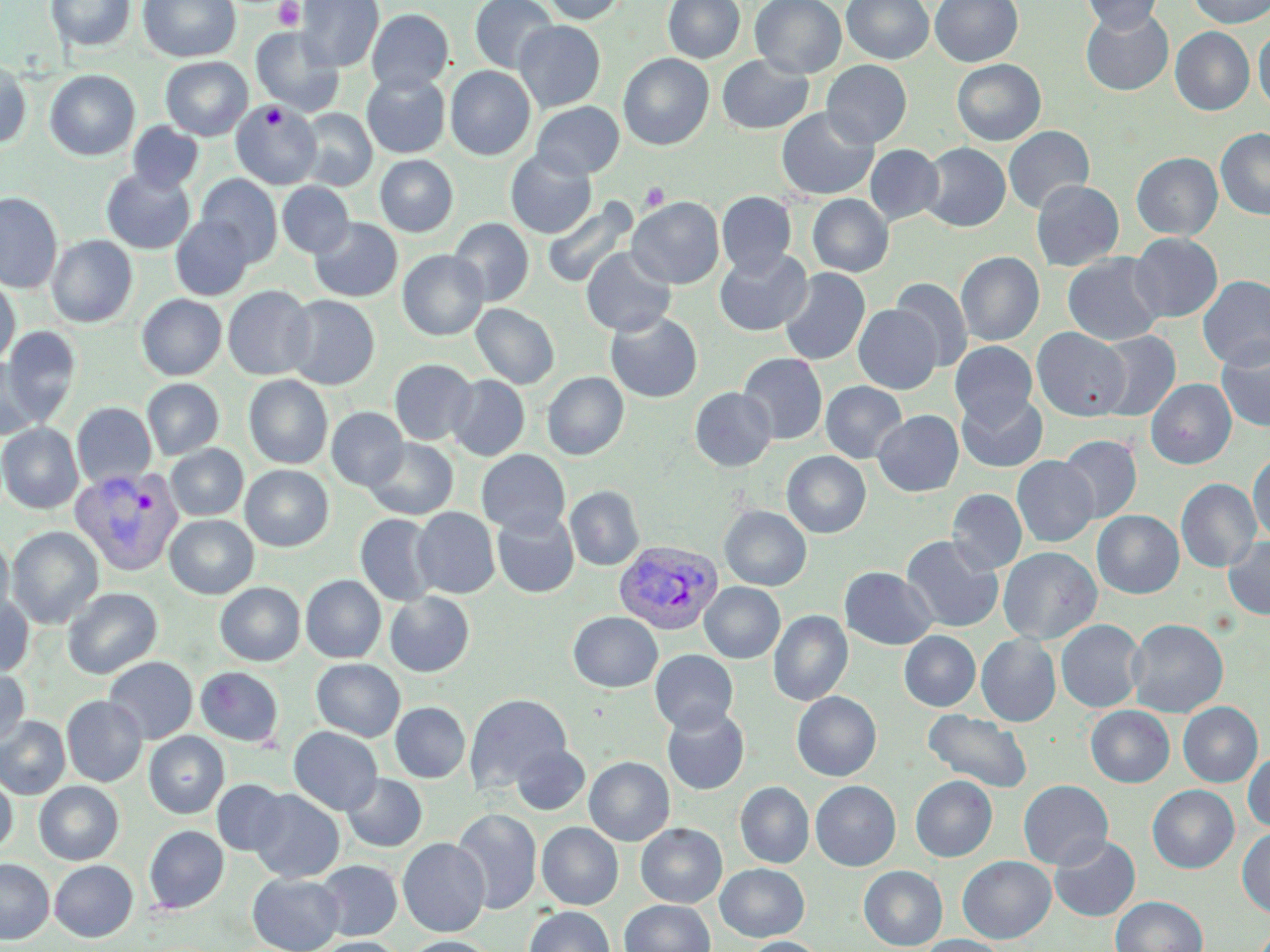

Summary:
  - Coordinate format: approximate bounding boxes as [x1, y1, x2, y2] in pixels
  - Uninfected red blood cell locations: [46, 0, 135, 52], [138, 0, 240, 62], [296, 0, 383, 71], [469, 0, 559, 73], [541, 0, 627, 24], [663, 0, 745, 63], [750, 0, 846, 78], [842, 0, 934, 64], [931, 0, 1023, 67], [1081, 0, 1164, 33], [1188, 0, 1270, 28], [1080, 6, 1174, 96], [366, 8, 453, 94], [514, 20, 606, 111], [251, 27, 345, 118], [1170, 27, 1254, 115], [1253, 27, 1270, 112], [618, 53, 714, 150], [716, 54, 815, 134], [160, 57, 252, 140], [951, 59, 1045, 146], [821, 60, 912, 148], [0, 61, 31, 148], [445, 66, 536, 160], [44, 69, 140, 161], [361, 72, 450, 158], [231, 101, 321, 189], [531, 101, 624, 178], [776, 107, 879, 200], [296, 108, 377, 191], [127, 122, 203, 193], [1004, 126, 1094, 214], [1215, 128, 1270, 220], [919, 143, 1010, 232], [864, 144, 944, 226], [505, 150, 597, 238], [1131, 152, 1223, 240], [375, 155, 458, 236], [101, 168, 195, 254], [195, 174, 283, 265], [1031, 180, 1124, 271], [277, 182, 355, 258], [717, 191, 796, 276], [0, 192, 63, 293], [807, 194, 893, 277], [627, 197, 724, 289], [542, 198, 638, 290], [170, 214, 255, 300], [309, 217, 402, 302], [449, 218, 534, 306], [1129, 232, 1222, 322], [47, 235, 138, 327], [581, 247, 677, 336], [398, 249, 489, 340], [715, 249, 813, 337], [956, 251, 1044, 346], [1062, 253, 1166, 346], [779, 267, 870, 365], [1198, 275, 1270, 370], [890, 277, 972, 373], [0, 278, 20, 366], [222, 285, 315, 380], [137, 294, 226, 380], [284, 295, 380, 389], [471, 303, 559, 389], [854, 304, 942, 394], [605, 311, 703, 403], [2, 326, 81, 425], [1031, 327, 1131, 421], [1094, 330, 1180, 421], [1216, 340, 1270, 432], [949, 341, 1037, 427], [738, 353, 828, 445], [0, 358, 42, 440], [389, 358, 478, 445], [542, 372, 629, 460], [447, 374, 529, 461], [244, 375, 333, 469], [142, 379, 224, 459], [1146, 379, 1236, 469], [821, 381, 907, 463], [690, 387, 777, 471], [957, 391, 1048, 472], [72, 402, 156, 488], [327, 407, 408, 491], [873, 410, 963, 497], [0, 422, 84, 514], [1058, 435, 1142, 524], [364, 438, 459, 519], [165, 444, 248, 520], [476, 449, 570, 537], [782, 451, 871, 538], [1248, 451, 1270, 544], [1012, 455, 1098, 547], [241, 464, 333, 551], [1176, 478, 1261, 573], [565, 485, 645, 571], [947, 489, 1027, 573], [719, 506, 811, 590], [412, 507, 500, 598], [1092, 510, 1183, 598], [492, 511, 579, 598], [355, 514, 439, 606], [164, 515, 259, 598], [7, 526, 104, 629], [0, 535, 14, 623], [901, 535, 1003, 632], [1222, 536, 1270, 620], [998, 546, 1102, 644], [840, 567, 937, 650], [301, 575, 386, 663], [215, 582, 305, 666], [699, 583, 785, 663], [62, 588, 161, 678], [385, 591, 474, 677], [0, 593, 34, 677], [768, 610, 852, 706], [568, 612, 663, 692], [1127, 618, 1228, 718], [1056, 619, 1146, 713], [900, 631, 980, 711], [976, 633, 1061, 726], [650, 649, 738, 733], [104, 657, 198, 743], [311, 659, 405, 741], [196, 667, 284, 747], [0, 668, 30, 747], [791, 691, 881, 781], [464, 693, 572, 793], [805, 694, 890, 869], [62, 695, 147, 786], [391, 702, 470, 783], [1178, 702, 1263, 787], [1086, 705, 1174, 787], [662, 706, 749, 795], [923, 710, 1033, 793], [0, 716, 70, 799], [289, 726, 383, 815], [144, 731, 229, 818], [510, 743, 590, 815], [1243, 750, 1270, 832], [584, 757, 674, 846], [0, 772, 16, 857], [342, 774, 427, 852], [911, 775, 997, 861], [212, 779, 291, 856], [1018, 780, 1113, 869], [34, 781, 123, 865], [811, 781, 900, 871], [735, 782, 814, 868], [1147, 785, 1239, 873], [248, 789, 344, 882], [451, 808, 542, 914], [537, 822, 623, 910], [636, 823, 727, 907], [144, 826, 229, 914], [1237, 827, 1270, 919], [1049, 835, 1141, 922], [398, 837, 490, 937], [957, 856, 1055, 943], [0, 859, 54, 944], [49, 860, 138, 942], [315, 860, 401, 940], [715, 863, 809, 941], [858, 865, 947, 950], [248, 873, 344, 951], [1111, 896, 1207, 952], [619, 899, 715, 952], [525, 906, 615, 952], [920, 935, 1005, 952], [402, 936, 496, 952], [315, 937, 404, 952], [743, 937, 825, 952]
  - Plasmodium vivax-infected red blood cell locations: [69, 465, 185, 575], [614, 540, 724, 635]
  - Platelet locations: [273, 0, 304, 30], [261, 105, 286, 127], [640, 182, 670, 211]
  - Slide-level diagnosis: Plasmodium vivax
  - Stain: May-Grünwald-Giemsa
  - Magnification: 1000x
  - Modality: light microscopy
  - Image size: 1270×952 pixels
  - Field of view: single
  - Preparation: thin blood film